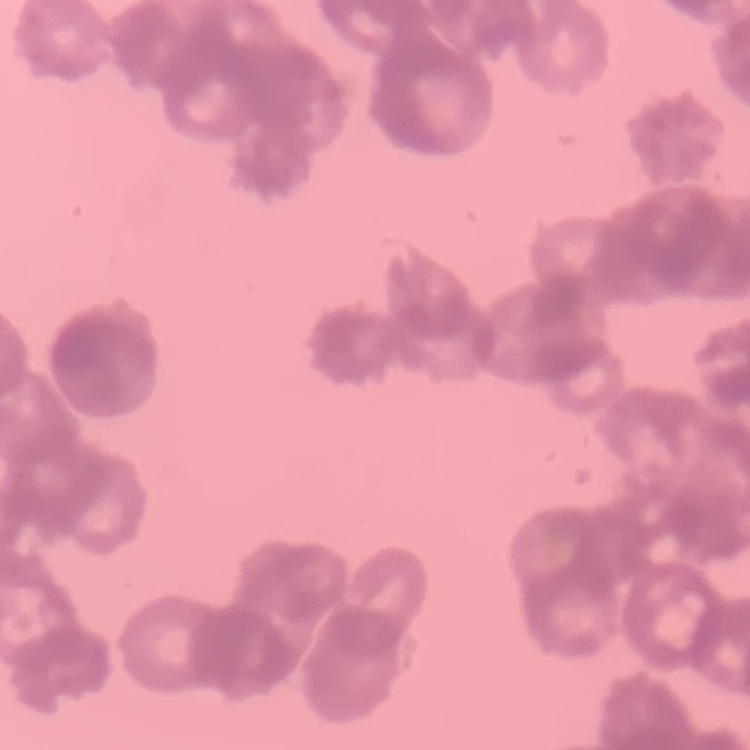

erythrocyte_morphology: rouleaux formation
stain: Field's or Giemsa
image_type: one tile cut from a larger photomicrograph
preparation: thin blood smear